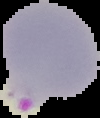

From a thin blood smear. Malaria status: parasitized. Image is 100×118 pixels. Segmented cell region on a black background.